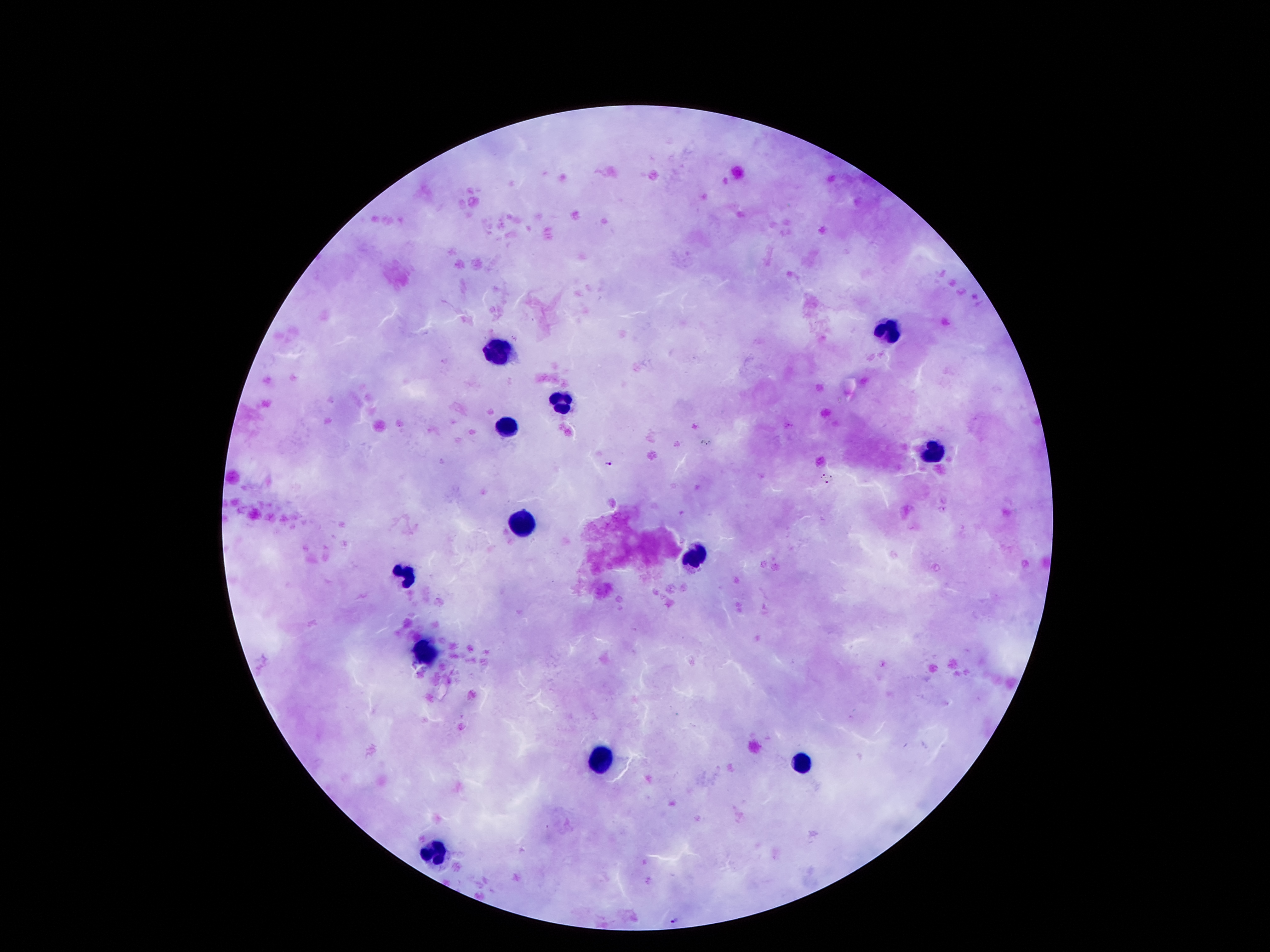
Approximate centers as [x, y] in pixels.
Summary:
  - Plasmodium parasite locations: [789, 425], [609, 463], [824, 474], [826, 482], [674, 919]
  - Leukocyte locations: [892, 333], [500, 354], [561, 407], [506, 426], [930, 451], [523, 524], [694, 555], [409, 573], [429, 649], [603, 757], [799, 763], [434, 851]
  - Field of view: single
  - Image size: 1270×952 pixels
  - Stain: Giemsa
  - Magnification: 100x
  - Capture: smartphone through the microscope eyepiece
  - Patient malaria status: infected with Plasmodium falciparum
  - Preparation: thick blood smear